Give the extent of all uninfected red blood cells.
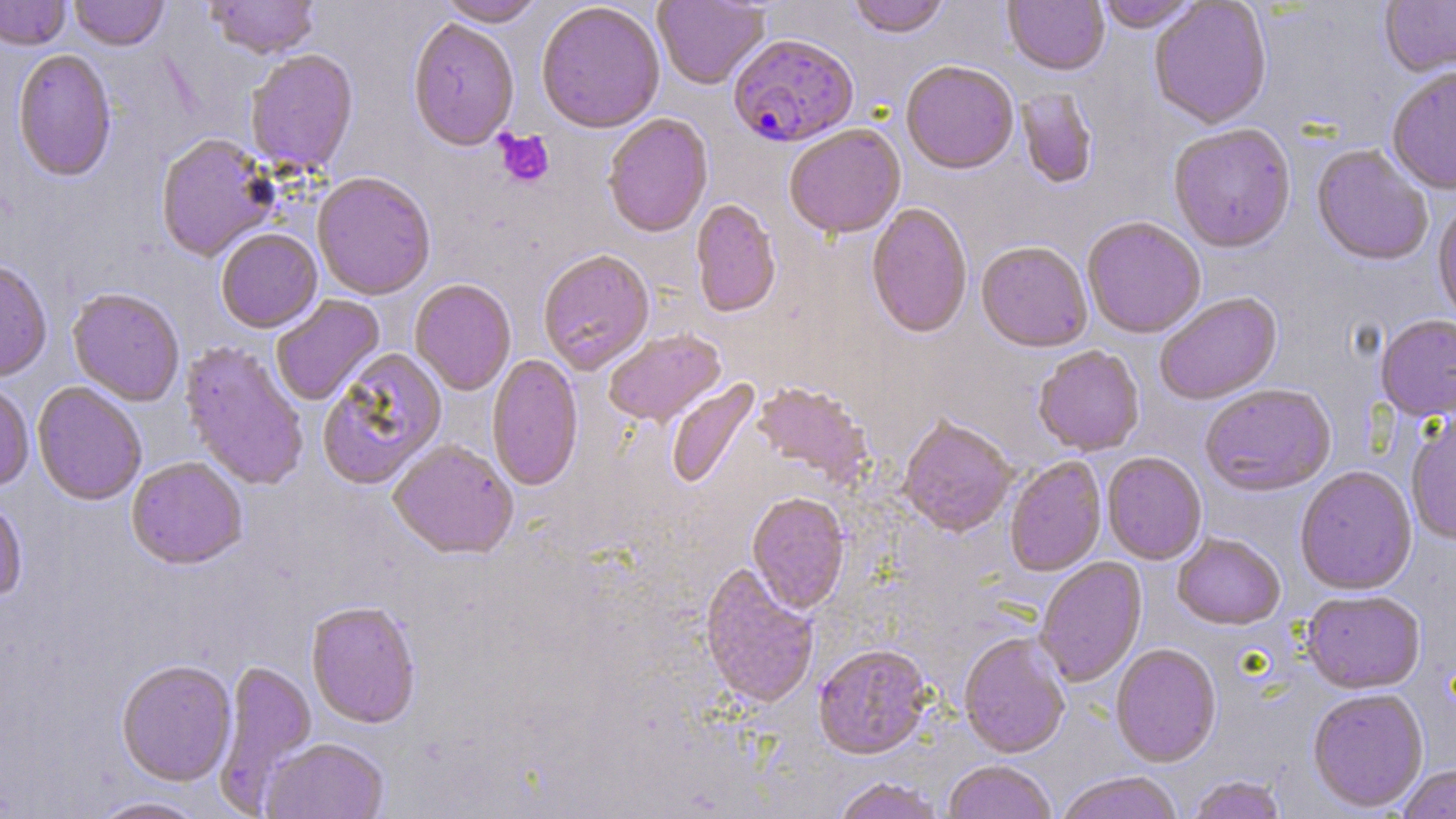

Approximate bounding boxes as (x1,y1)-(x2,y2) corner pairs in pixels.
Uninfected red blood cells: (0,0)-(71,52), (69,0)-(169,53), (207,0)-(319,61), (436,0)-(545,29), (652,0)-(770,91), (849,0)-(949,41), (1003,0)-(1109,78), (1096,0)-(1203,35), (1380,0)-(1456,79), (1149,1)-(1272,132), (537,4)-(665,136), (407,21)-(519,154), (12,52)-(117,183), (245,52)-(359,177), (901,63)-(1019,177), (1386,70)-(1456,197), (1016,88)-(1098,191), (603,115)-(713,241), (1169,126)-(1296,256), (784,127)-(906,242), (156,134)-(277,263), (1312,145)-(1431,268), (312,175)-(436,302), (691,200)-(781,319), (1432,204)-(1456,326), (866,205)-(973,340), (1082,219)-(1205,340), (216,230)-(323,334), (975,244)-(1092,355), (538,251)-(654,376), (0,262)-(51,384), (410,280)-(516,396), (67,290)-(184,407), (271,295)-(386,406), (1155,295)-(1283,407), (1376,316)-(1456,424), (604,331)-(727,429), (179,343)-(308,491), (1033,348)-(1145,458), (318,350)-(449,493), (487,354)-(583,493), (666,379)-(763,491), (32,383)-(147,507), (752,383)-(873,487), (0,384)-(34,493), (1200,386)-(1338,499), (1406,413)-(1456,547), (898,419)-(1017,539), (388,442)-(518,563), (1102,454)-(1207,566), (1005,458)-(1107,578), (126,459)-(247,573), (1295,468)-(1417,598), (747,495)-(850,616), (0,500)-(27,605), (1172,535)-(1285,632), (1036,558)-(1147,688), (698,565)-(818,711), (1301,593)-(1426,696), (306,603)-(421,730), (959,635)-(1070,760), (813,646)-(932,762), (1110,646)-(1221,768), (213,660)-(318,813), (116,662)-(237,788), (1307,690)-(1429,815), (261,739)-(390,819), (944,762)-(1056,819), (1397,764)-(1456,819), (1056,773)-(1182,819), (1187,776)-(1288,819), (833,777)-(944,819), (88,796)-(210,819).

Plasmodium falciparum-infected red blood cell locations: (728,36)-(859,151). Platelet locations: (495,129)-(555,188). Slide-level diagnosis: Plasmodium falciparum. 1000x magnification. Thin blood smear. Image is 1456×819 pixels. May-Grünwald-Giemsa stain. Single field of view. Light microscopy.